Give the extent of all uninfected red blood cells.
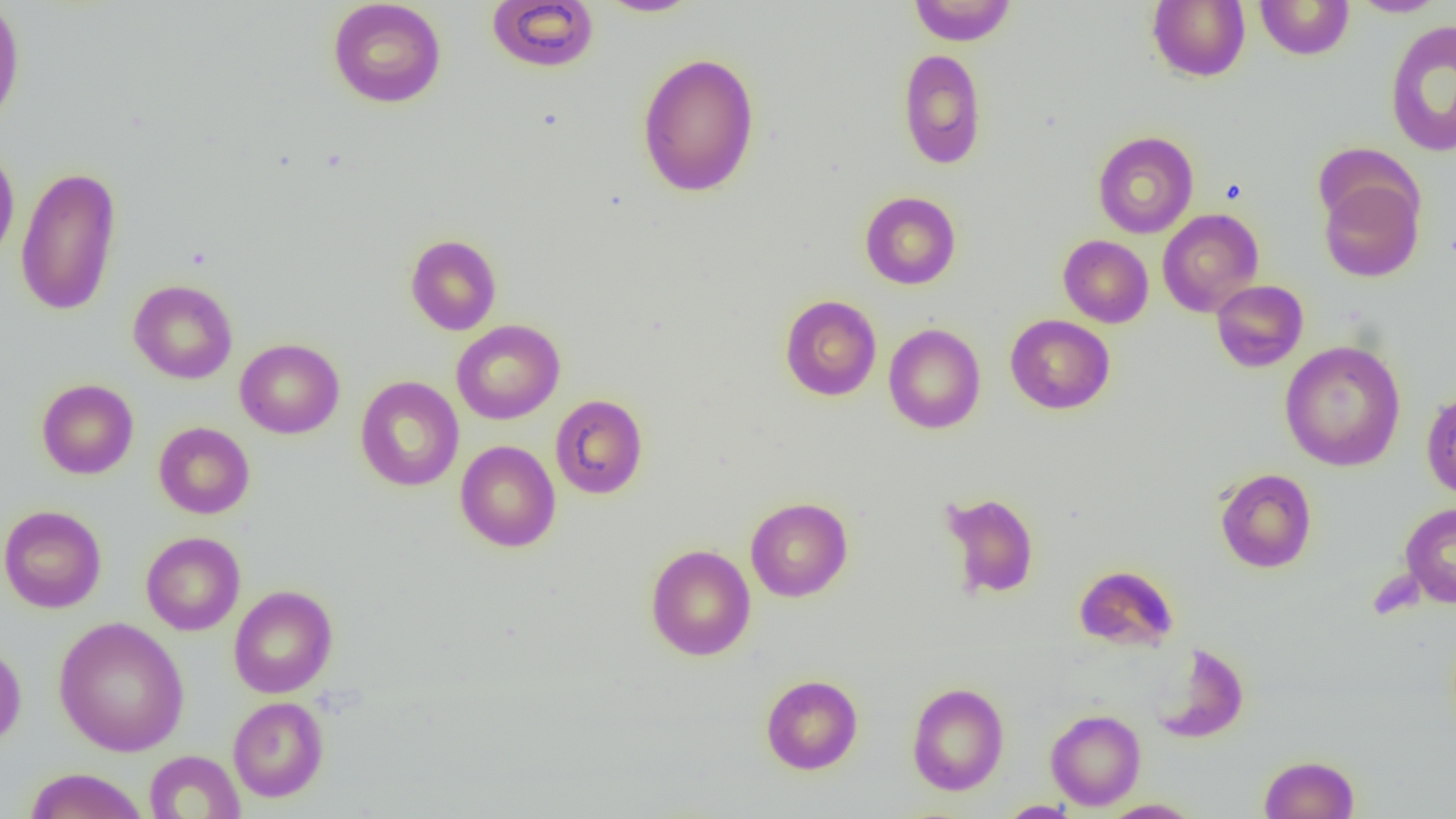

Approximate bounding boxes as [x1, y1, x2, y2] in pixels.
Uninfected red blood cells: [0, 0, 25, 129], [596, 0, 703, 17], [909, 0, 1017, 46], [1147, 0, 1250, 82], [1254, 0, 1354, 60], [328, 1, 447, 108], [487, 1, 600, 72], [1350, 1, 1450, 17], [1385, 18, 1456, 157], [897, 47, 986, 169], [636, 51, 761, 197], [1092, 131, 1199, 238], [0, 143, 20, 267], [15, 164, 122, 318], [1318, 177, 1424, 282], [860, 191, 961, 289], [1157, 209, 1265, 317], [405, 234, 502, 335], [1058, 235, 1154, 328], [128, 279, 238, 384], [1211, 280, 1308, 372], [779, 295, 882, 401], [1005, 314, 1115, 414], [451, 320, 565, 424], [883, 323, 986, 434], [235, 338, 344, 439], [1280, 340, 1406, 471], [355, 375, 464, 491], [36, 379, 138, 479], [1421, 386, 1456, 501], [550, 394, 648, 499], [153, 422, 254, 518], [455, 440, 561, 552], [1215, 468, 1317, 573], [940, 491, 1040, 600], [745, 497, 853, 602], [1400, 503, 1456, 607], [0, 505, 107, 613], [141, 531, 245, 635], [645, 543, 756, 661], [1074, 565, 1179, 652], [228, 585, 338, 698], [53, 617, 190, 757], [0, 642, 26, 748], [1151, 642, 1250, 743], [761, 674, 863, 774], [906, 682, 1009, 795], [228, 696, 329, 802], [1045, 709, 1145, 810], [144, 751, 245, 818], [1259, 754, 1360, 818], [23, 768, 148, 819], [1099, 799, 1204, 818], [997, 801, 1081, 818].

slide_level_diagnosis: no evidence of blood parasites
field_of_view: single
image_size: 1456×819 pixels
modality: optical microscopy
magnification: 1000x
preparation: thin blood film